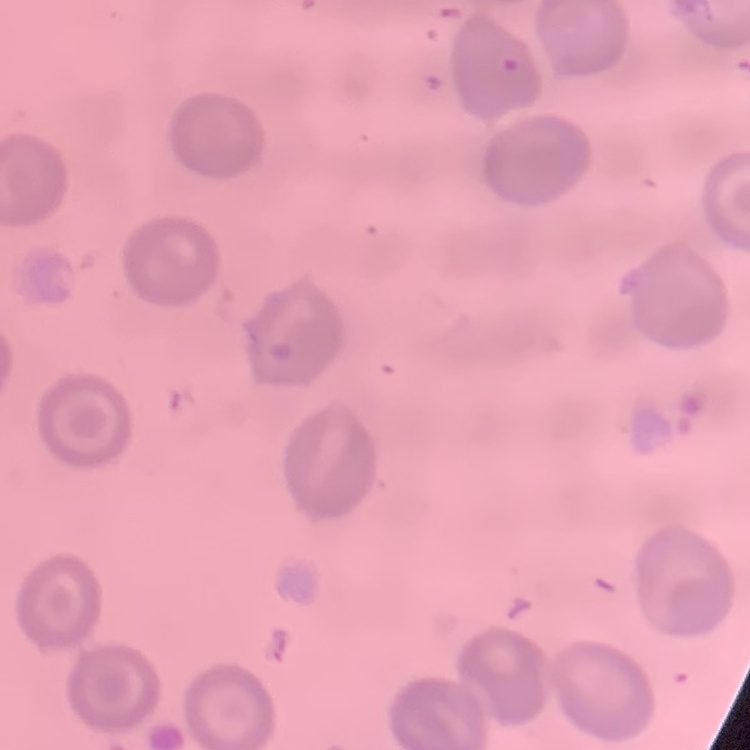

{
  "erythrocyte_morphology": "no rouleaux formation",
  "preparation": "thin blood film",
  "image_type": "one tile cut from a larger photomicrograph",
  "stain": "Field's or Giemsa"
}